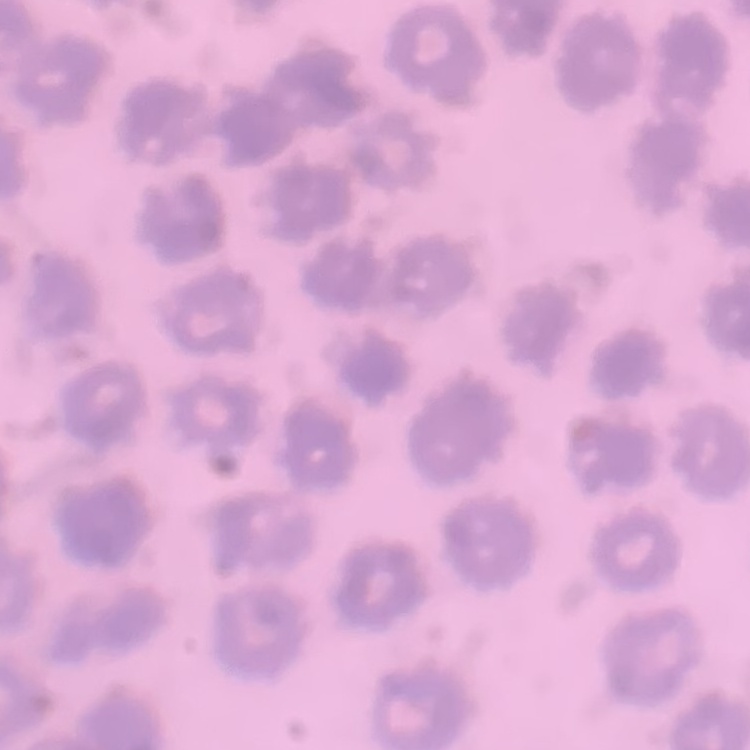 The erythrocytes exhibit no rouleaux formation. Thin blood film. Square crop of a larger photomicrograph. Field's or Giemsa stain.